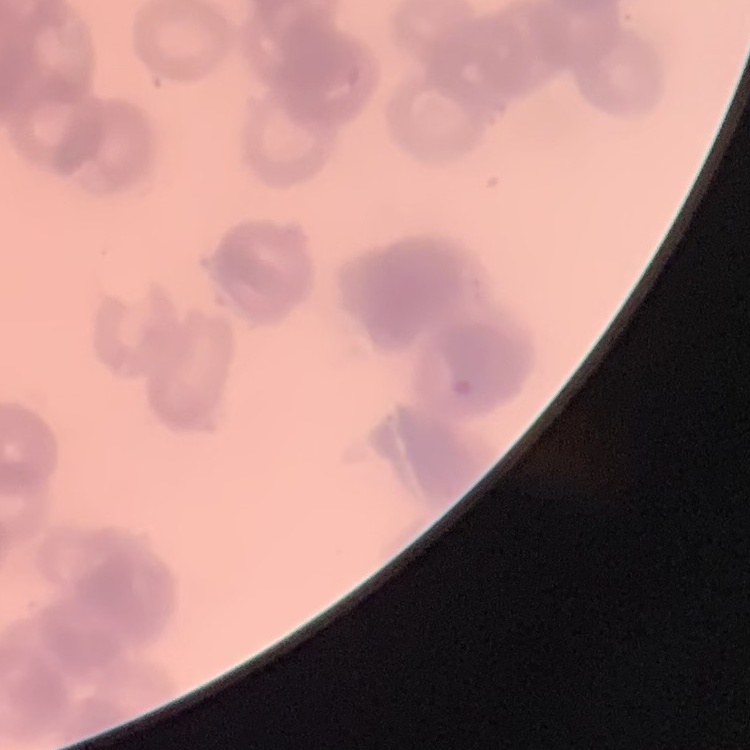

Summary:
  - Red blood cell morphology: rouleaux formation
  - Image type: one tile cut from a larger photomicrograph
  - Stain: Field's or Giemsa
  - Preparation: thin blood film